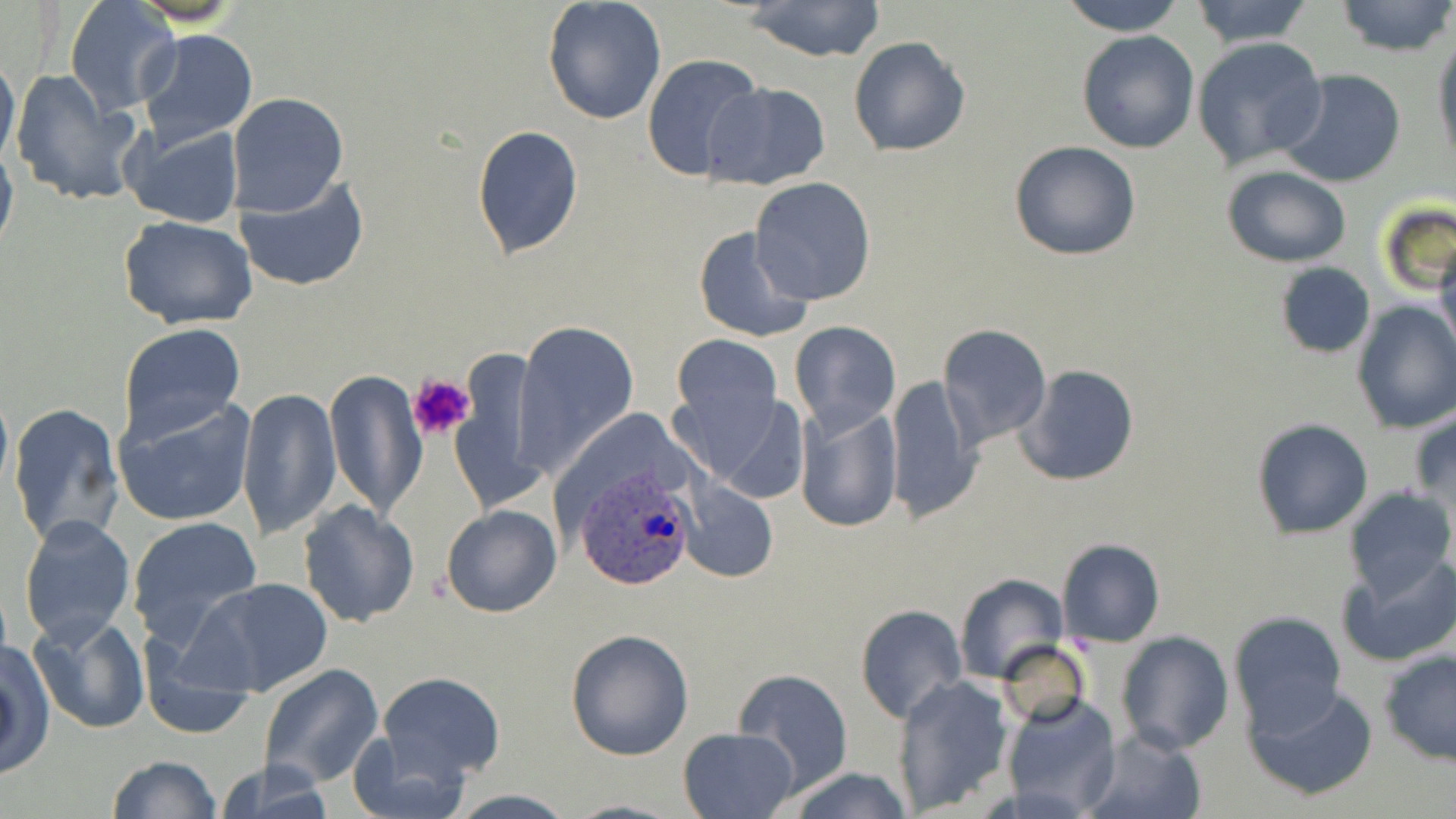
Summary:
  - Coordinate format: approximate bounding boxes as (x1, y1, x2, y2) in pixels
  - Platelet locations: (407, 372, 474, 444)
  - Uninfected red blood cell locations: (739, 0, 887, 63), (1059, 0, 1186, 34), (1187, 0, 1317, 48), (1333, 0, 1456, 57), (64, 1, 178, 116), (542, 2, 668, 124), (136, 28, 259, 150), (1076, 30, 1199, 153), (1431, 32, 1455, 170), (847, 35, 970, 158), (1191, 37, 1327, 170), (0, 48, 20, 174), (642, 53, 765, 183), (11, 68, 145, 206), (1276, 69, 1407, 188), (703, 82, 831, 192), (226, 92, 348, 217), (123, 122, 244, 229), (473, 125, 584, 258), (0, 136, 18, 260), (1010, 141, 1140, 260), (1222, 166, 1350, 267), (233, 173, 370, 292), (750, 178, 877, 304), (1377, 198, 1456, 297), (119, 216, 260, 330), (693, 225, 816, 342), (1433, 241, 1456, 362), (1275, 263, 1376, 358), (1352, 301, 1456, 434), (789, 321, 901, 433), (515, 322, 638, 473), (118, 323, 247, 445), (939, 323, 1052, 446), (670, 333, 783, 456), (1017, 364, 1140, 488), (325, 369, 425, 517), (885, 375, 982, 524), (237, 387, 342, 541), (115, 396, 257, 527), (8, 403, 125, 549), (793, 403, 903, 534), (1408, 406, 1456, 511), (1250, 417, 1374, 539), (681, 478, 778, 584), (1342, 488, 1455, 602), (297, 501, 420, 627), (442, 504, 561, 618), (20, 514, 135, 646), (129, 517, 261, 649), (1056, 538, 1164, 646), (1339, 553, 1456, 668), (953, 573, 1069, 685), (185, 576, 335, 699), (854, 603, 967, 725), (29, 611, 147, 733), (1228, 611, 1346, 732), (564, 629, 695, 760), (1116, 632, 1234, 754), (998, 639, 1089, 728), (0, 642, 55, 784), (1378, 650, 1456, 765), (259, 663, 384, 789), (731, 668, 854, 793), (377, 671, 505, 782), (896, 675, 1013, 814), (1245, 685, 1378, 802), (1004, 691, 1124, 816), (678, 727, 800, 818), (1081, 728, 1207, 819), (347, 729, 469, 819), (106, 755, 222, 819), (213, 760, 335, 819), (786, 766, 912, 819), (444, 790, 578, 819), (562, 797, 687, 819)
  - Plasmodium ovale-infected red blood cell locations: (571, 460, 701, 592)
  - Slide-level diagnosis: Plasmodium ovale
  - Magnification: 1000x
  - Preparation: thin blood smear
  - Stain: May-Grünwald-Giemsa
  - Modality: optical microscopy
  - Field of view: single
  - Image size: 1456×819 pixels